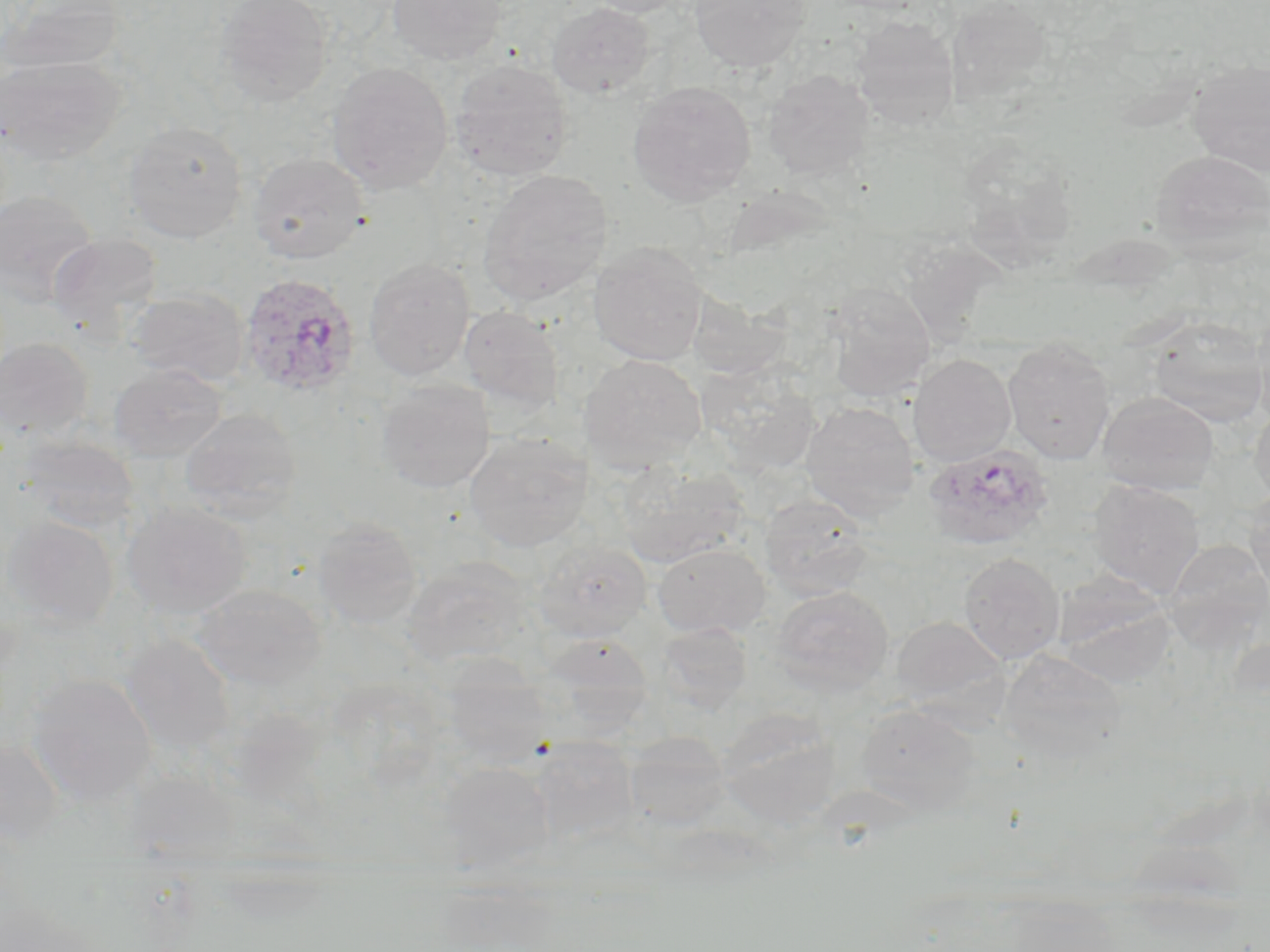
slide-level diagnosis = Plasmodium ovale
preparation = thin blood film
modality = optical microscopy
uninfected red blood cell locations = approximate bounding boxes as named x1/y1/x2/y2 corners in pixels: (x1=1, y1=0, x2=127, y2=74), (x1=214, y1=0, x2=333, y2=106), (x1=386, y1=0, x2=509, y2=65), (x1=578, y1=0, x2=697, y2=18), (x1=689, y1=0, x2=811, y2=72), (x1=946, y1=1, x2=1051, y2=104), (x1=546, y1=2, x2=656, y2=98), (x1=850, y1=17, x2=960, y2=130), (x1=0, y1=55, x2=125, y2=166), (x1=449, y1=59, x2=573, y2=182), (x1=1188, y1=60, x2=1270, y2=177), (x1=326, y1=62, x2=454, y2=194), (x1=763, y1=70, x2=875, y2=180), (x1=627, y1=80, x2=757, y2=206), (x1=124, y1=121, x2=248, y2=243), (x1=970, y1=147, x2=1077, y2=283), (x1=1150, y1=148, x2=1270, y2=256), (x1=248, y1=153, x2=369, y2=264), (x1=478, y1=169, x2=613, y2=307), (x1=0, y1=190, x2=97, y2=307), (x1=47, y1=232, x2=163, y2=332), (x1=588, y1=242, x2=708, y2=366), (x1=364, y1=257, x2=475, y2=380), (x1=824, y1=283, x2=935, y2=401), (x1=126, y1=288, x2=249, y2=386), (x1=459, y1=306, x2=565, y2=415), (x1=1146, y1=317, x2=1268, y2=427), (x1=0, y1=337, x2=93, y2=439), (x1=1003, y1=338, x2=1115, y2=464), (x1=581, y1=353, x2=707, y2=471), (x1=909, y1=354, x2=1016, y2=466), (x1=109, y1=363, x2=227, y2=461), (x1=702, y1=368, x2=823, y2=476), (x1=375, y1=378, x2=495, y2=493), (x1=1098, y1=391, x2=1218, y2=495), (x1=800, y1=401, x2=918, y2=521), (x1=1249, y1=404, x2=1270, y2=507), (x1=179, y1=407, x2=302, y2=520), (x1=464, y1=432, x2=592, y2=552), (x1=18, y1=435, x2=139, y2=534), (x1=617, y1=464, x2=750, y2=567), (x1=1088, y1=480, x2=1204, y2=599), (x1=1243, y1=488, x2=1270, y2=597), (x1=760, y1=493, x2=876, y2=601), (x1=121, y1=501, x2=252, y2=619), (x1=2, y1=515, x2=119, y2=629), (x1=313, y1=517, x2=423, y2=630), (x1=533, y1=539, x2=651, y2=640), (x1=1162, y1=541, x2=1269, y2=652), (x1=653, y1=543, x2=770, y2=637), (x1=959, y1=552, x2=1064, y2=664), (x1=402, y1=559, x2=532, y2=667), (x1=1054, y1=575, x2=1175, y2=686), (x1=195, y1=584, x2=327, y2=689), (x1=770, y1=586, x2=894, y2=697), (x1=890, y1=615, x2=1007, y2=711), (x1=657, y1=622, x2=752, y2=713), (x1=122, y1=633, x2=237, y2=756), (x1=543, y1=633, x2=655, y2=723), (x1=999, y1=649, x2=1126, y2=764), (x1=442, y1=659, x2=553, y2=768), (x1=26, y1=672, x2=156, y2=805), (x1=857, y1=704, x2=981, y2=816), (x1=718, y1=709, x2=841, y2=829), (x1=623, y1=731, x2=730, y2=831), (x1=531, y1=736, x2=640, y2=845), (x1=0, y1=738, x2=65, y2=843), (x1=439, y1=761, x2=555, y2=863), (x1=125, y1=769, x2=240, y2=857), (x1=0, y1=886, x2=103, y2=952)
Plasmodium ovale-infected red blood cell locations = approximate bounding boxes as named x1/y1/x2/y2 corners in pixels: (x1=238, y1=272, x2=360, y2=397), (x1=923, y1=443, x2=1055, y2=551)
magnification = 1000x
image size = 1270×952 pixels
field of view = single
stain = May-Grünwald-Giemsa